Assess for malaria.
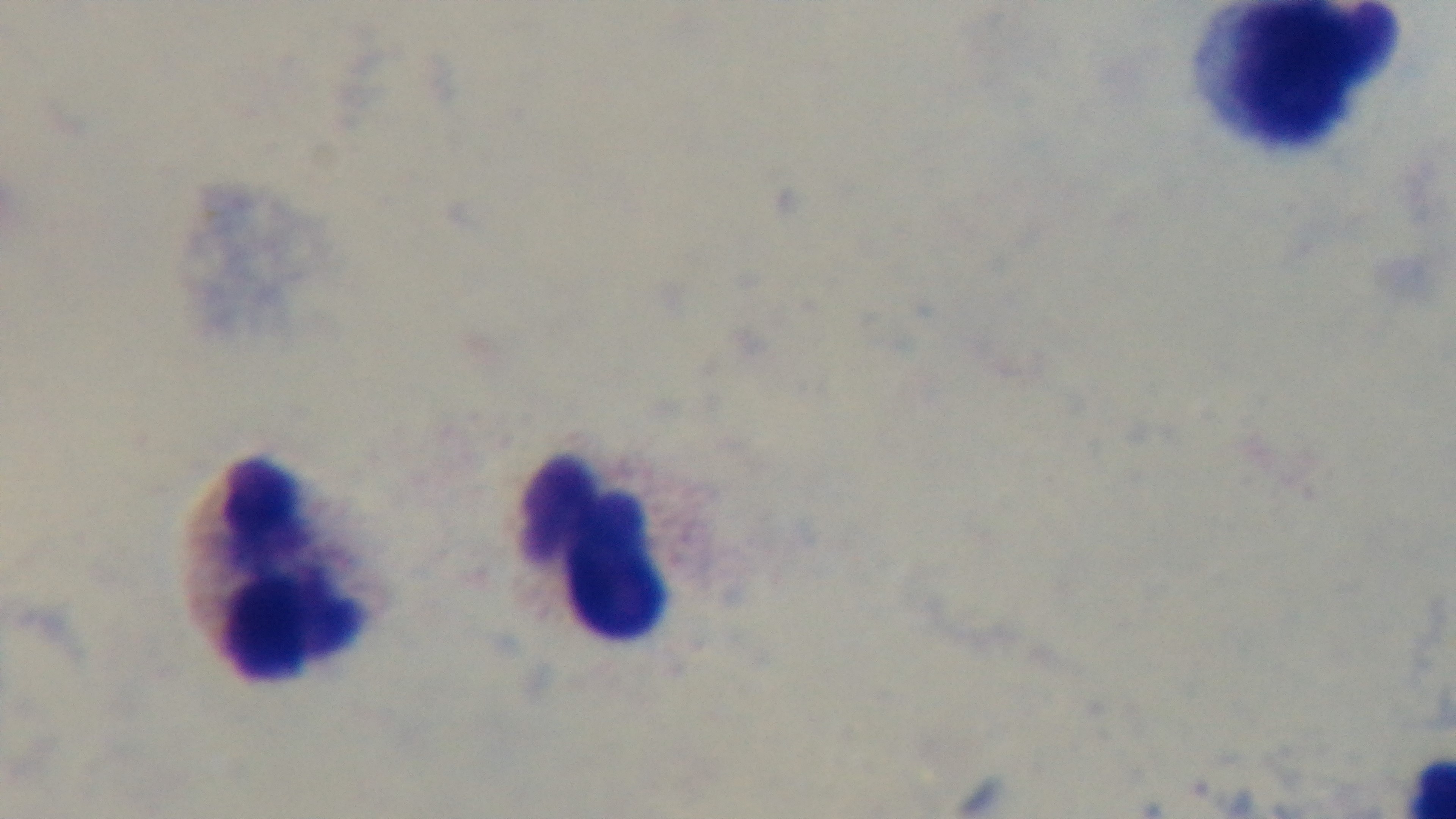

It is uninfected.

Summary:
  - Objective: 100x oil immersion
  - Capture: mounted 4K digital camera
  - Stain: Giemsa
  - Field of view: one from the slide
  - Preparation: thick
  - Modality: light microscopy